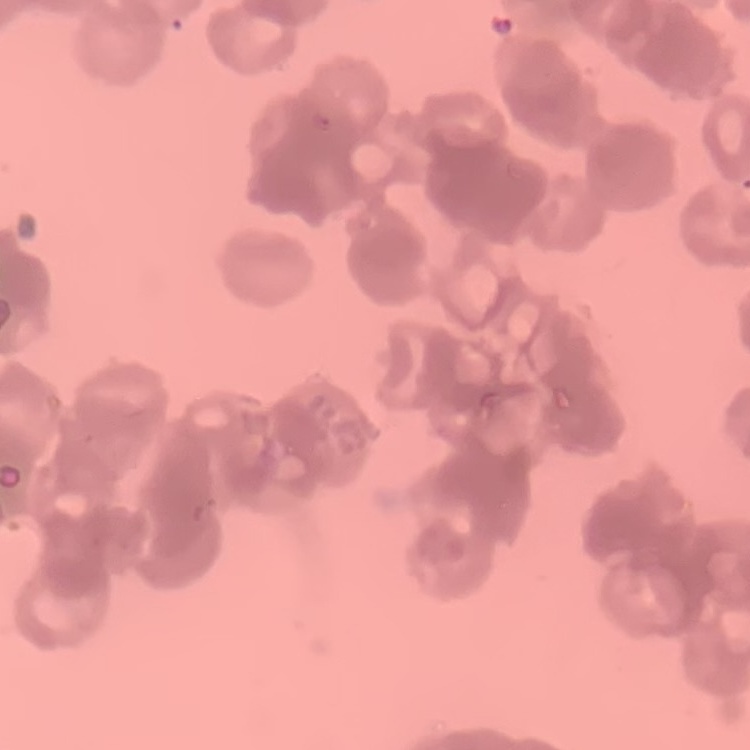
red blood cell morphology = rouleaux formation
image type = one tile cut from a larger photomicrograph
stain = Field's or Giemsa
preparation = thin peripheral smear